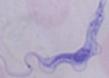
Summary:
  - Identification: trypanosome
  - Magnification: 1000x
  - Modality: photomicrograph